Identify the preparation type.
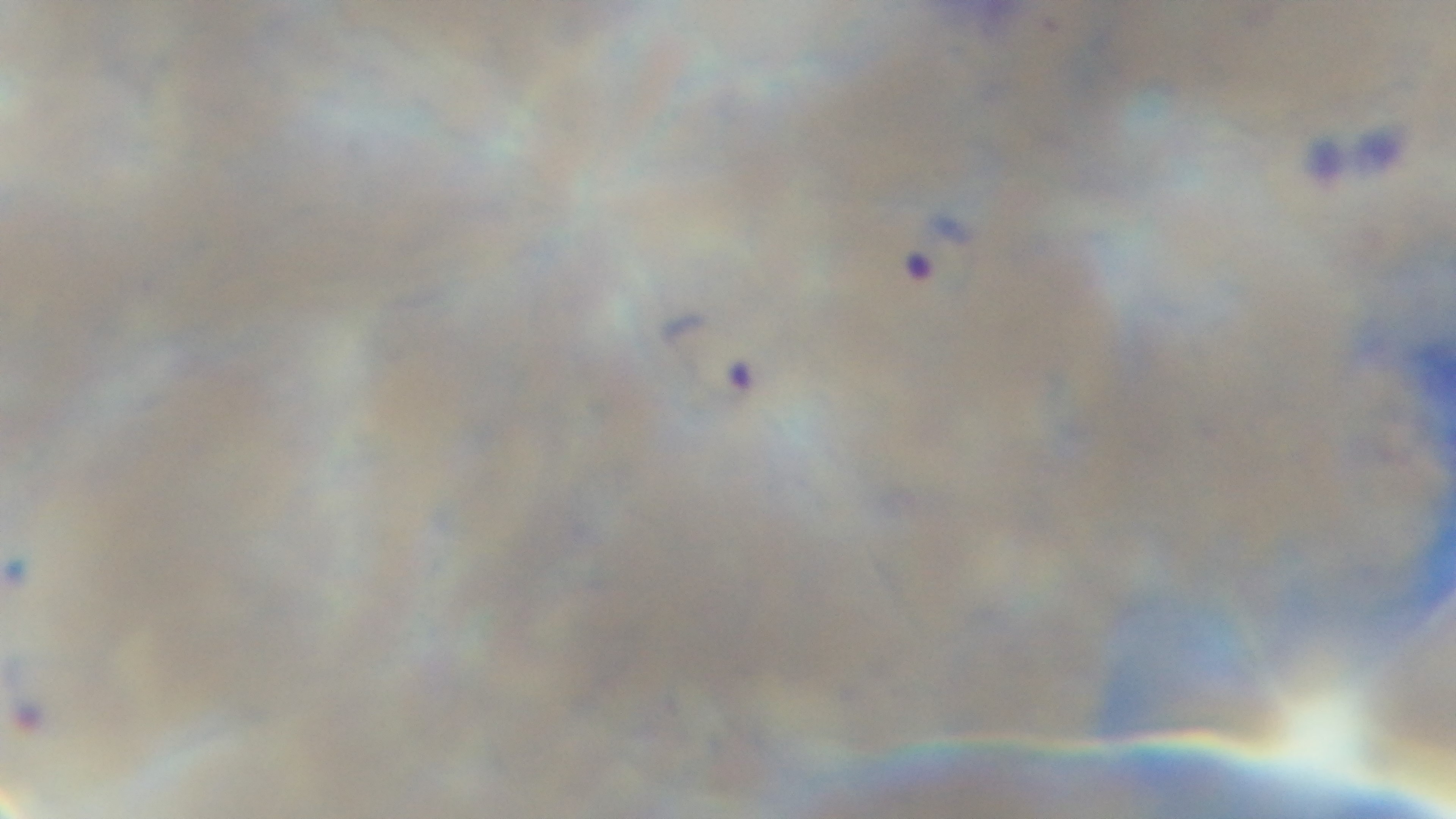
Thin.

Summary:
  - Modality: light microscopy
  - Stain: Giemsa
  - Field of view: one from the slide
  - Malaria status: infected
  - Capture: mounted 4K digital camera
  - Objective: 100x oil immersion